Mark where platelets are.
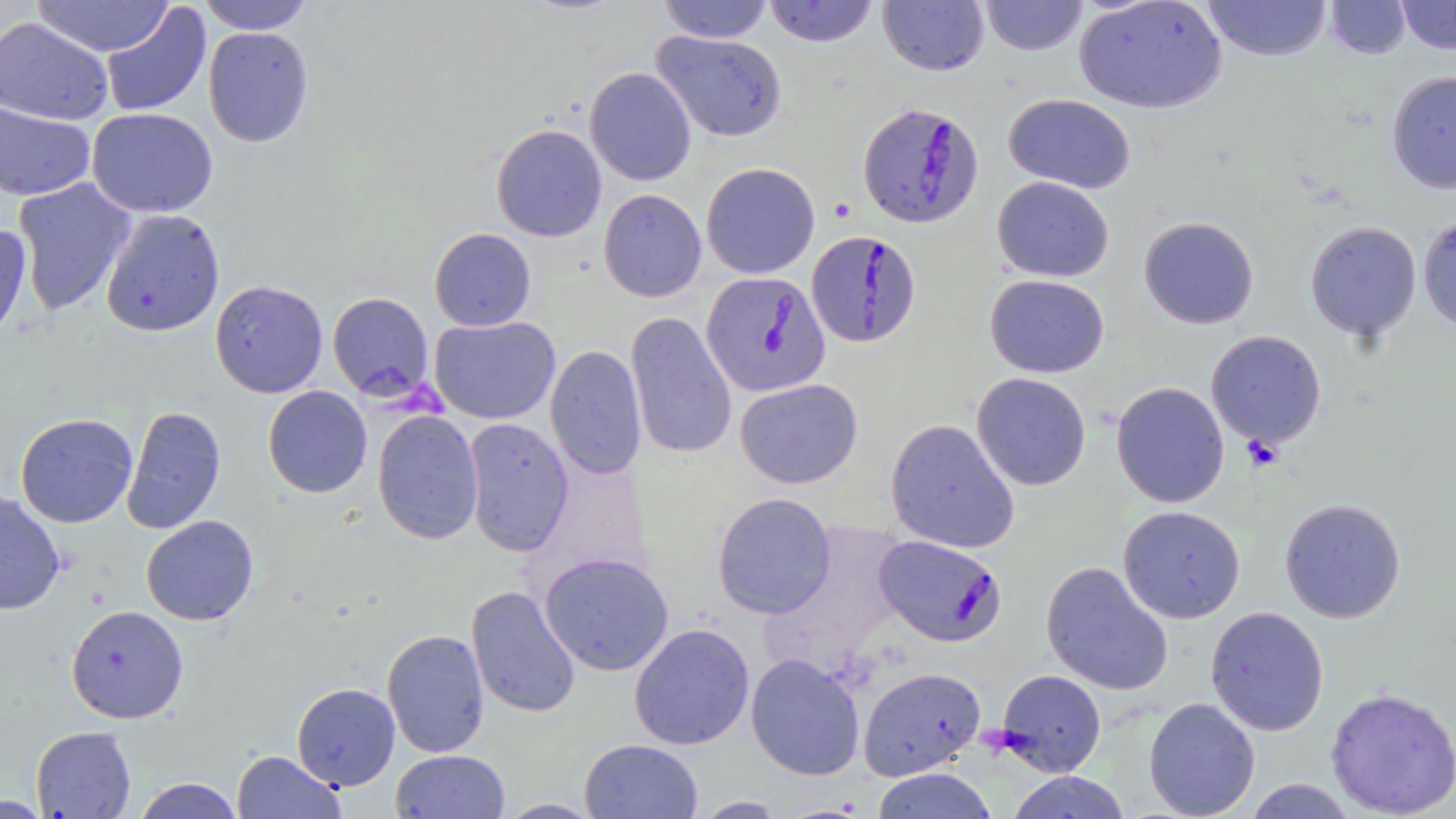

Approximate bounding boxes as (x1, y1, x2, y2) in pixels.
Platelets: (1241, 435, 1284, 471).

Plasmodium falciparum-infected red blood cell locations: (857, 102, 984, 228), (806, 230, 920, 347), (701, 271, 830, 397), (874, 535, 1006, 646). Uninfected red blood cell locations: (32, 0, 175, 57), (198, 0, 315, 34), (658, 0, 774, 43), (763, 0, 879, 47), (878, 0, 989, 76), (979, 0, 1088, 56), (1203, 0, 1333, 62), (1325, 0, 1412, 60), (1395, 0, 1456, 54), (1074, 1, 1227, 114), (100, 3, 212, 118), (0, 16, 113, 125), (203, 25, 314, 148), (651, 30, 788, 142), (585, 66, 696, 186), (1386, 69, 1456, 195), (1004, 93, 1136, 194), (0, 99, 95, 201), (86, 107, 218, 218), (491, 124, 607, 242), (701, 162, 820, 278), (992, 176, 1114, 282), (12, 177, 137, 315), (599, 188, 706, 302), (99, 208, 225, 337), (1417, 213, 1456, 332), (1139, 216, 1259, 329), (1305, 221, 1422, 340), (0, 224, 32, 348), (429, 228, 536, 331), (985, 274, 1109, 377), (210, 280, 328, 398), (327, 292, 434, 400), (626, 311, 737, 460), (429, 316, 560, 424), (1206, 330, 1327, 448), (545, 344, 645, 481), (972, 372, 1091, 491), (735, 378, 863, 489), (1111, 381, 1230, 508), (263, 385, 372, 498), (121, 405, 226, 534), (372, 410, 484, 544), (15, 412, 138, 528), (463, 418, 574, 556), (885, 418, 1019, 553), (0, 490, 65, 615), (712, 492, 836, 619), (1279, 497, 1406, 623), (1117, 505, 1246, 624), (141, 515, 258, 626), (539, 552, 674, 676), (1041, 561, 1173, 696), (466, 585, 581, 719), (66, 605, 188, 723), (1205, 606, 1329, 736), (629, 623, 755, 750), (382, 628, 490, 758), (746, 653, 865, 781), (857, 666, 986, 780), (995, 669, 1107, 777), (292, 682, 400, 790), (1325, 686, 1456, 818), (1143, 696, 1260, 819), (31, 726, 136, 818), (579, 738, 702, 818), (232, 750, 346, 818), (392, 750, 510, 819), (870, 767, 997, 819), (1005, 771, 1132, 819), (133, 777, 244, 818), (1243, 778, 1357, 818), (0, 795, 52, 817), (691, 796, 787, 818), (497, 799, 603, 818). Slide-level diagnosis: Plasmodium falciparum. 1000x magnification. May-Grünwald-Giemsa-stained preparation. Light microscopy. Thin blood smear. One field of a larger specimen. Image is 1456×819 pixels.